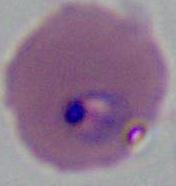 Photomicrograph. Captured at either 400x or 1000x magnification. A Plasmodium parasite is seen.